Give the position of every leukocyte visible.
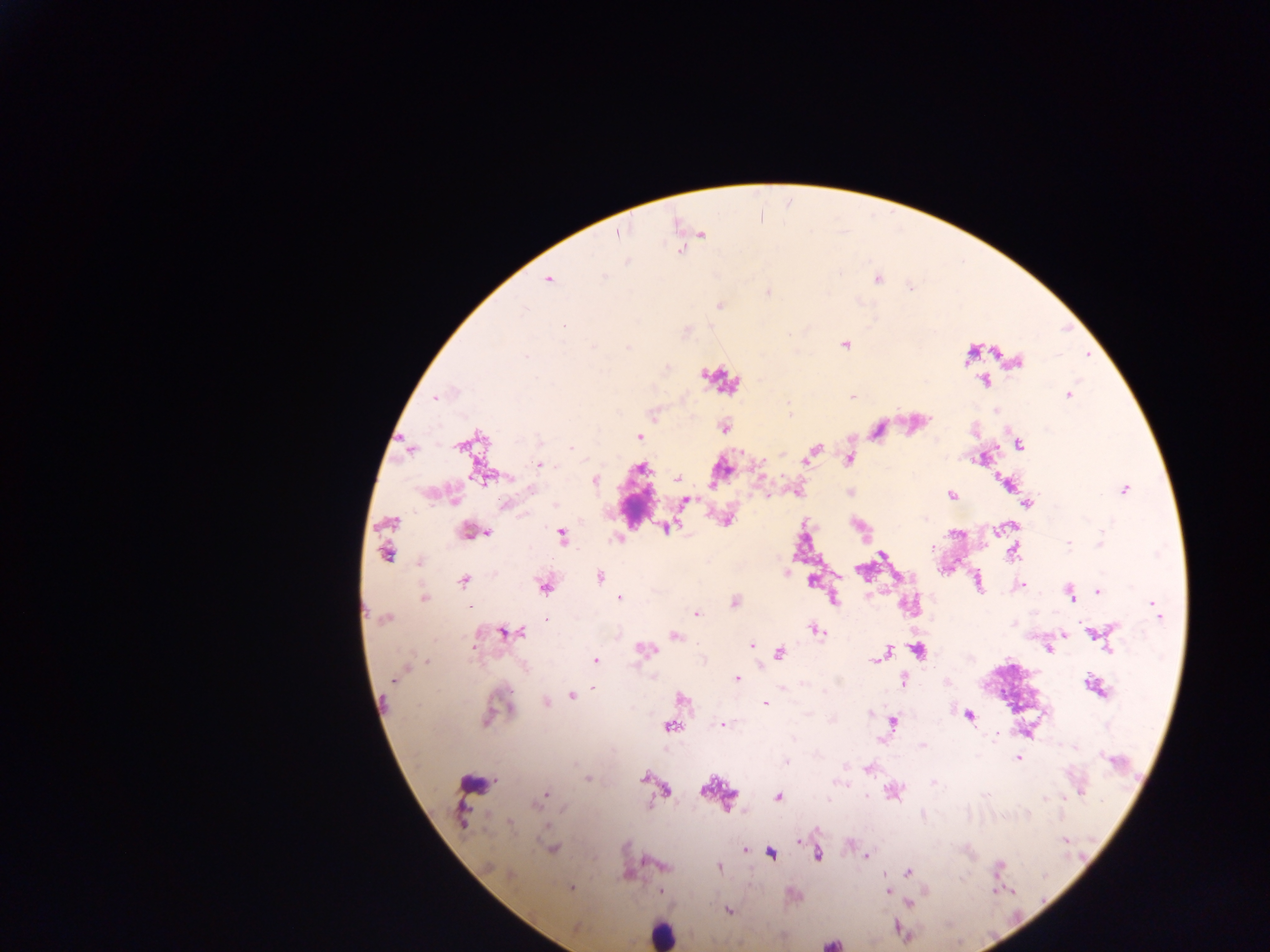

Approximate centers as (x, y) in pixels.
Leukocytes: (719, 379), (472, 784), (662, 933).
One object is labeled both malaria parasite and leukocyte by the source: (831, 943).

image size = 1270×952 pixels
country = Ghana
capture = mobile-phone photograph through a microscope
preparation = thick blood smear
malaria parasite locations = approximate centers as (x, y) in pixels: (617, 231), (700, 235), (547, 280), (767, 292), (845, 344), (996, 352), (969, 353), (1017, 360), (985, 380), (1068, 395), (435, 397), (852, 397), (789, 415), (723, 427), (875, 430), (639, 436), (468, 442), (1018, 444), (813, 450), (848, 459), (539, 465), (642, 465), (481, 475), (677, 479), (595, 480), (1007, 482), (1123, 489), (797, 491), (851, 492), (952, 495), (685, 501), (1027, 503), (726, 518), (1011, 526), (665, 528), (999, 529), (469, 531), (487, 532), (562, 535), (1067, 543), (386, 551), (1013, 551), (882, 554), (418, 562), (786, 572), (599, 577), (812, 579), (464, 580), (977, 582), (1020, 585), (544, 586), (1099, 591), (1070, 592), (619, 597), (423, 598), (833, 598), (735, 602), (1156, 610), (695, 613), (384, 618), (817, 629), (506, 632), (1064, 633), (1099, 633), (674, 635), (751, 645), (1048, 648), (645, 649), (917, 650), (778, 653), (883, 654), (595, 660), (399, 673), (735, 678), (901, 681), (593, 686), (1093, 686), (572, 695), (681, 698), (545, 701), (765, 704), (495, 710), (969, 715), (892, 721), (722, 724), (670, 725), (1017, 757), (868, 768), (589, 778), (644, 778), (658, 787), (665, 789), (892, 789), (544, 794), (778, 796), (508, 822), (798, 841), (551, 848), (744, 850), (771, 853), (816, 854), (866, 856), (662, 865), (717, 866), (907, 872), (570, 887), (661, 891), (887, 892), (908, 903), (727, 910), (576, 928)
field of view = single